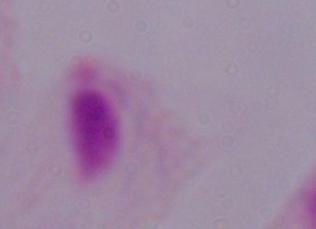

{
  "magnification": "1000x",
  "modality": "photomicrograph",
  "identification": "trichomonad"
}